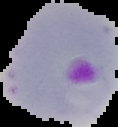
Summary:
  - Image type: segmented cell region with the area outside set to black
  - Preparation: thin blood smear
  - Malaria status: parasitized
  - Image size: 118×127 pixels